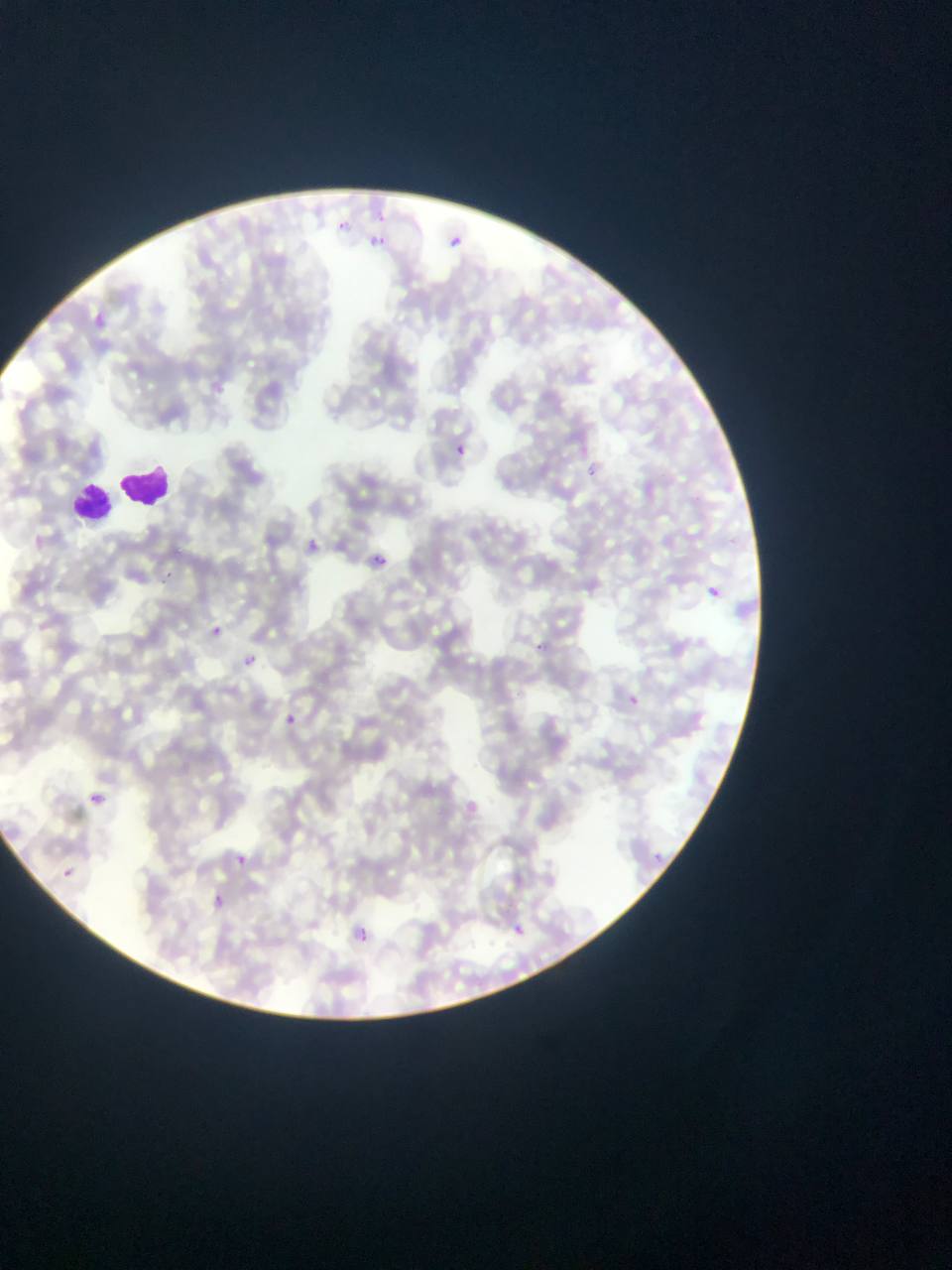
Approximate bounding boxes as (left, top, right, bottom) in pixels.
Summary:
  - Leukocyte locations: (123, 461, 171, 512), (71, 479, 116, 520)
  - Plasmodium parasite locations: (376, 206, 390, 225), (334, 216, 350, 231), (443, 225, 476, 253), (371, 232, 392, 257), (88, 311, 113, 328), (448, 438, 474, 474), (582, 461, 607, 489), (302, 532, 323, 560), (365, 542, 400, 582), (164, 571, 174, 583), (711, 575, 729, 606), (203, 619, 220, 643), (524, 627, 545, 657), (235, 652, 259, 666), (620, 688, 650, 713), (284, 709, 299, 728), (88, 791, 105, 805), (650, 843, 663, 858), (232, 847, 250, 868), (63, 868, 73, 878), (210, 890, 227, 905), (349, 922, 378, 952), (512, 923, 528, 938)
  - Preparation: thin blood smear
  - Capture: mobile-phone photograph through a microscope
  - Country: Ghana
  - Image size: 952×1270 pixels
  - Field of view: single